Give the extent of all uninfected red blood cells.
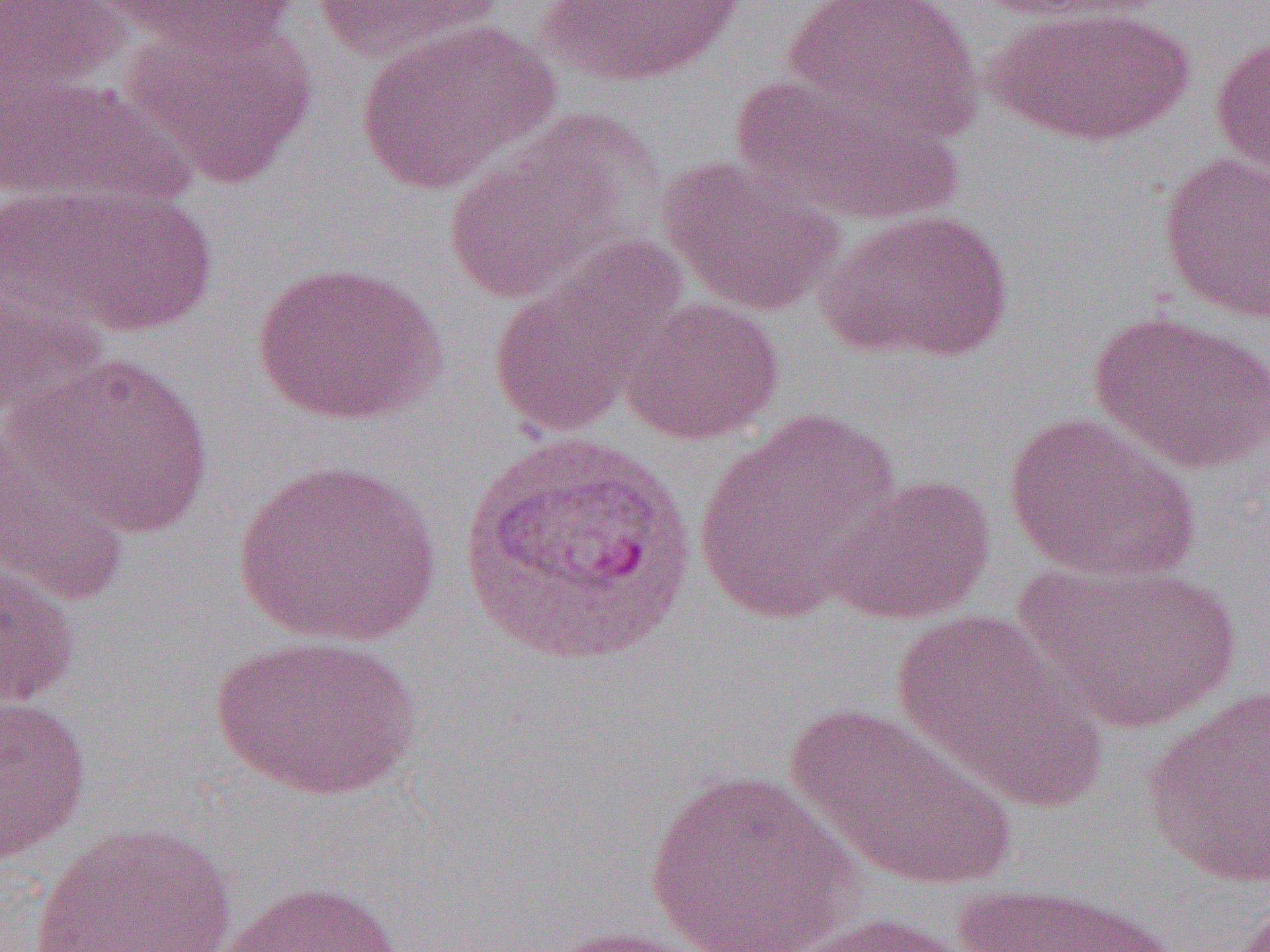
Approximate bounding boxes as (x1, y1, x2, y2) in pixels.
Uninfected red blood cells: (0, 0, 130, 111), (98, 0, 298, 58), (308, 0, 502, 65), (540, 0, 743, 86), (781, 0, 982, 141), (965, 0, 1147, 22), (983, 4, 1196, 148), (122, 19, 318, 188), (355, 20, 558, 193), (1210, 30, 1270, 178), (0, 71, 190, 211), (727, 73, 964, 225), (440, 126, 640, 306), (1157, 151, 1270, 324), (659, 155, 845, 316), (16, 185, 219, 337), (816, 209, 1014, 365), (487, 240, 684, 440), (250, 260, 447, 427), (0, 274, 108, 424), (619, 296, 784, 445), (1090, 309, 1269, 475), (15, 352, 215, 540), (694, 408, 902, 623), (1003, 411, 1200, 584), (0, 419, 137, 607), (234, 458, 442, 647), (827, 473, 996, 624), (0, 560, 82, 711), (1015, 560, 1239, 734), (890, 606, 1104, 809), (209, 633, 421, 800), (1141, 687, 1270, 888), (0, 694, 92, 863), (784, 701, 1018, 892), (643, 767, 863, 952), (27, 823, 238, 951), (220, 881, 405, 952), (948, 881, 1184, 952), (780, 911, 973, 952), (532, 924, 721, 952).

slide-level diagnosis = Plasmodium vivax
magnification = 1000x
preparation = thin blood smear
modality = light microscopy
field of view = single
image size = 1270×952 pixels